Report the malaria status of this cell.
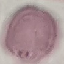
It is uninfected.

Automatically extracted cell patch, resized to 64 × 64 pixels. Giemsa-stained preparation. Thin blood smear. Acquired by smartphone through the microscope eyepiece.